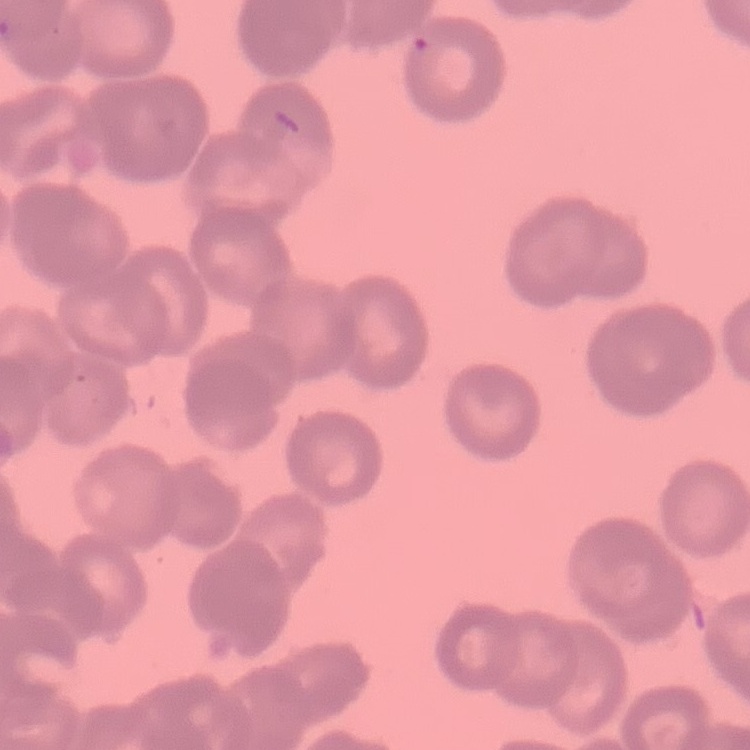
Summary:
  - Red blood cell morphology: rouleaux formation
  - Image type: square crop of a larger photomicrograph
  - Preparation: thin peripheral smear
  - Stain: Field's or Giemsa